Locate every Plasmodium parasite and every leukocyte.
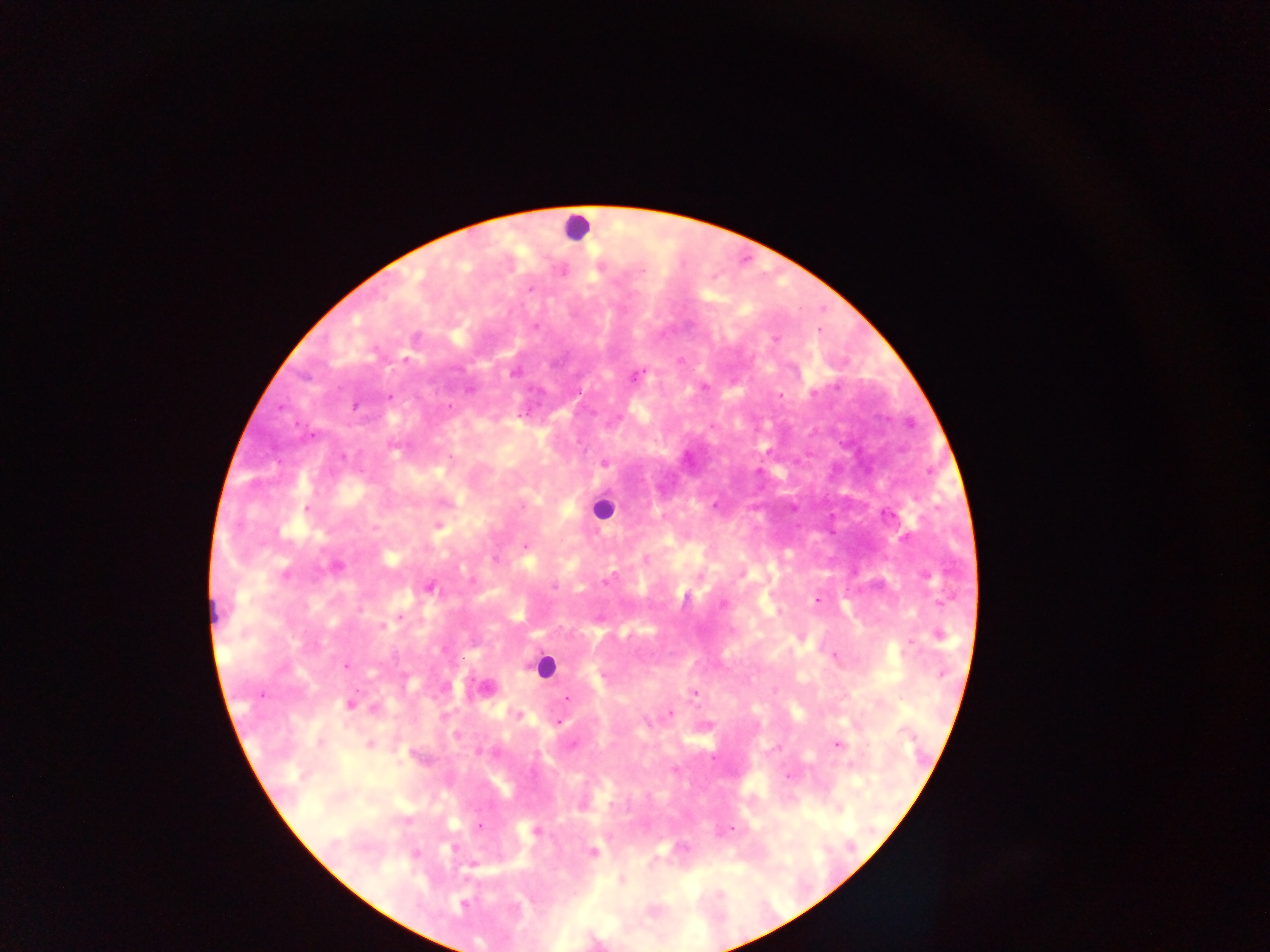
Approximate centers as x y in pixels.
Plasmodium parasites: 642 271; 530 289; 535 327; 776 340; 406 360; 514 372; 635 376; 703 387; 470 390; 813 393; 389 396; 780 396; 354 406; 448 407; 604 463; 522 506; 307 508; 439 526; 525 546; 337 566; 286 574; 926 576; 608 579; 554 586; 429 587; 685 596; 817 600; 940 603; 722 605; 401 618; 383 627; 940 635; 910 644; 834 657; 346 666; 942 673; 603 676; 693 693; 260 695; 568 698; 350 705; 375 708; 670 713; 519 714; 557 723; 456 735; 369 744; 573 745; 837 745; 790 777; 479 825; 732 827; 535 831; 453 849; 592 852; 473 865; 621 881; 463 904.
Leukocytes: 577 227; 600 509; 544 666.

Summary:
  - Field of view: single
  - Capture: mobile-phone photograph through a microscope
  - Country: Ghana
  - Preparation: thick blood smear
  - Image size: 1270×952 pixels